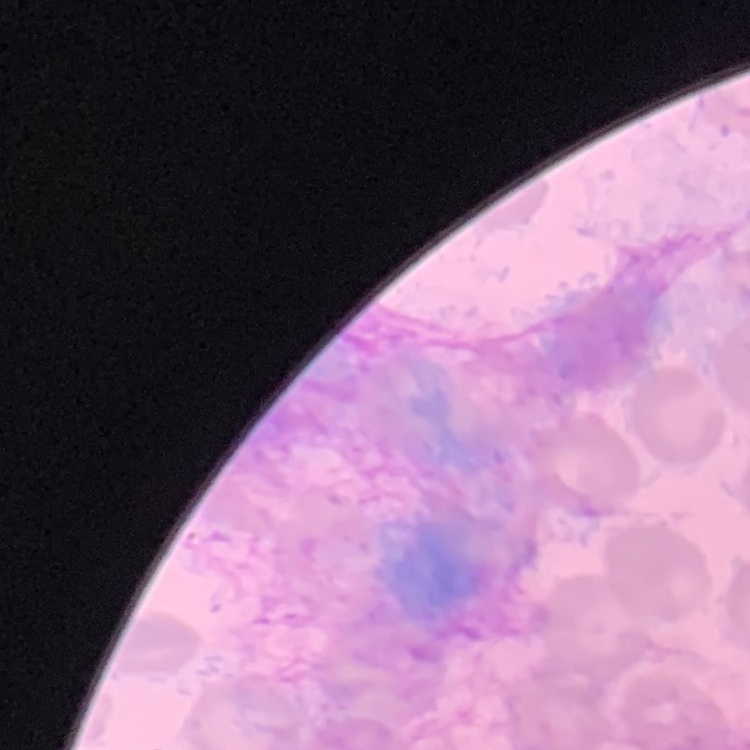
The red blood cells show no rouleaux formation. Thin peripheral smear. Square crop of a larger photomicrograph. Field's or Giemsa stain.